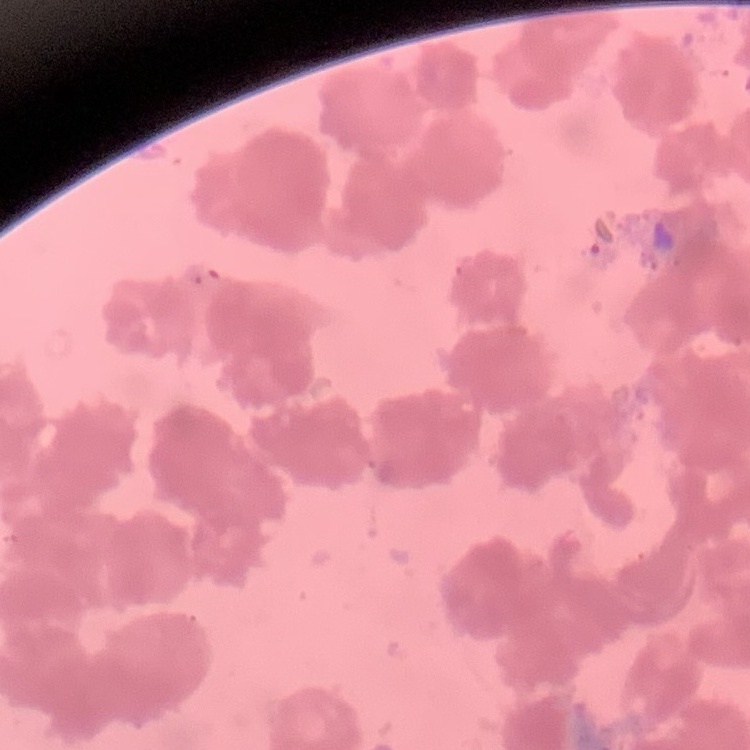

Summary:
  - Erythrocyte morphology: rouleaux formation
  - Preparation: thin blood smear
  - Stain: Field's or Giemsa
  - Image type: one tile cut from a larger photomicrograph